Report the malaria status of this cell.
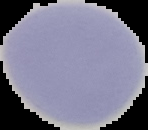

Uninfected.

Image is 148×130 pixels. From a thin blood smear. The area outside the segmented cell region is set to black.